Identify the parasite.
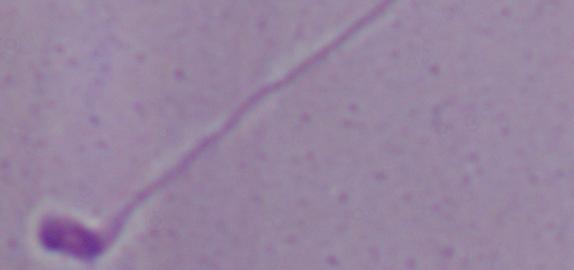

Leishmania.

1000x magnification. Micrograph.